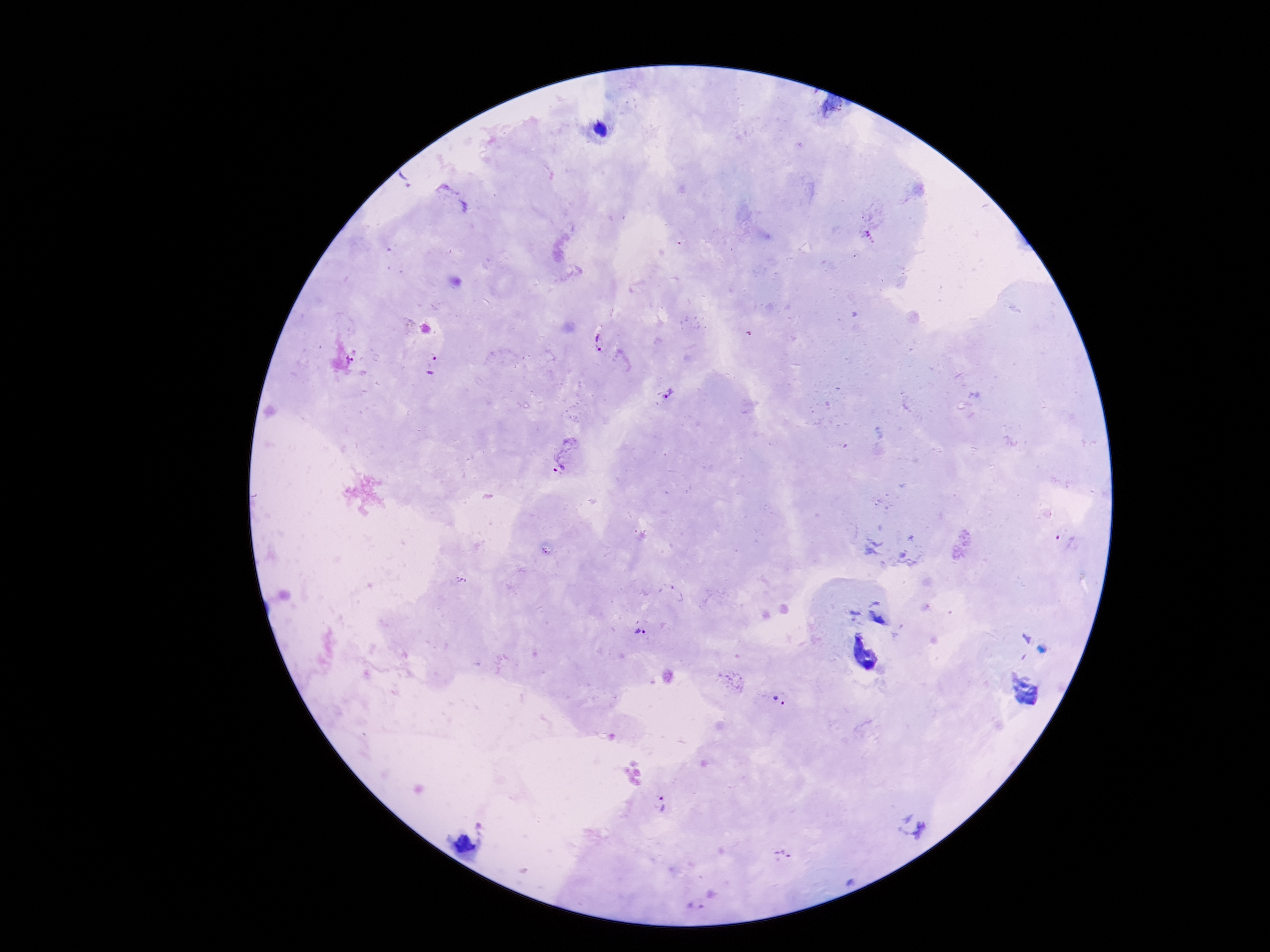

field of view = single
magnification = 100x
preparation = thick blood smear
capture = smartphone camera through the microscope eyepiece
Plasmodium parasite locations = approximate object centers, in pixels from the top-left corner: (x=406, y=179), (x=599, y=343), (x=356, y=356), (x=432, y=365), (x=666, y=394), (x=563, y=453), (x=1066, y=540), (x=639, y=633), (x=778, y=701), (x=661, y=804), (x=782, y=856), (x=695, y=906)
image size = 1270×952 pixels
patient malaria status = infected
stain = Giemsa